Locate every blood parasite and identify its species.
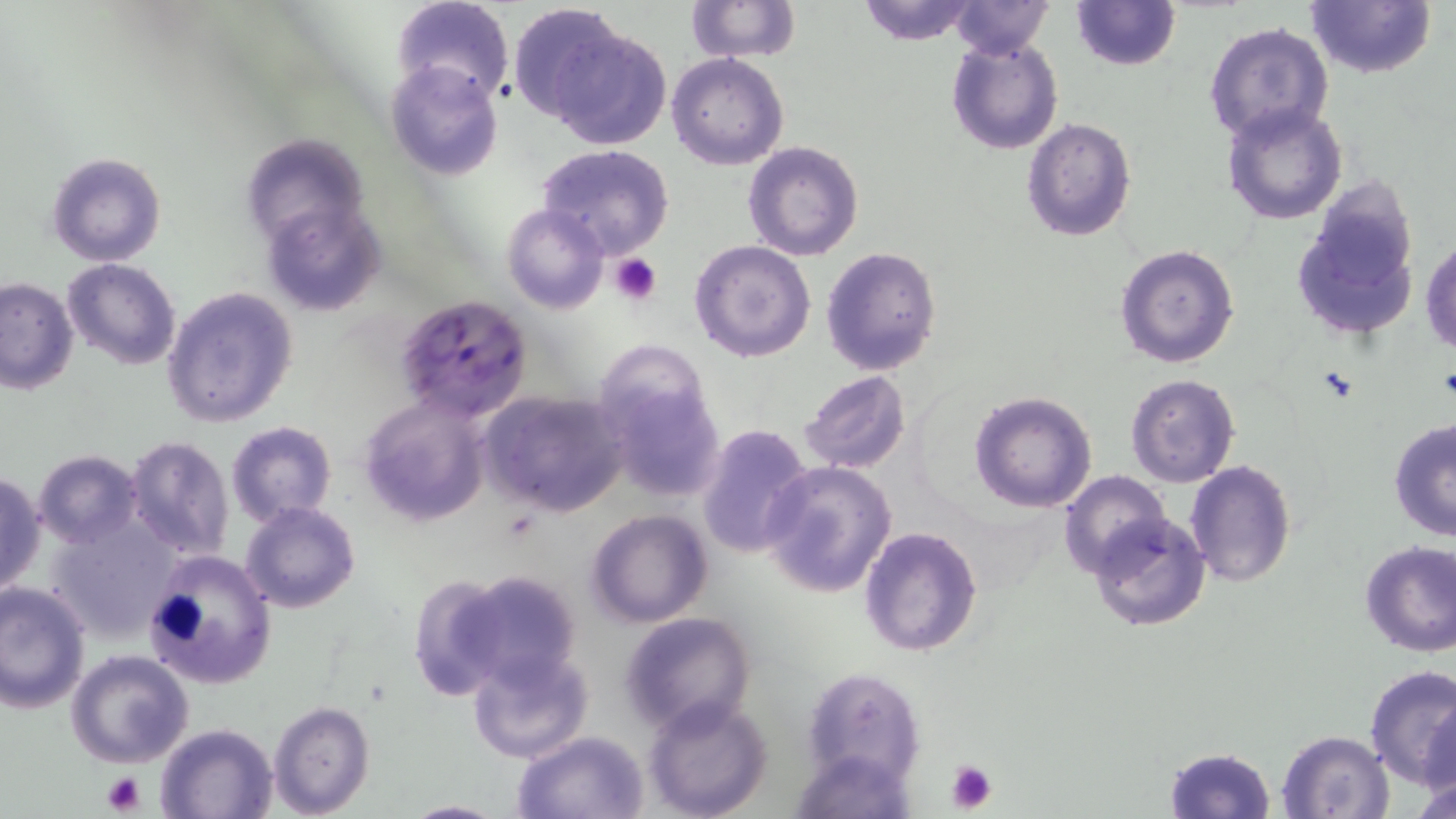
Approximate bounding boxes as [x1, y1, x2, y2] in pixels.
Plasmodium falciparum-infected red blood cells: [396, 294, 533, 422].
No Plasmodium ovale, Plasmodium malariae, Plasmodium vivax, Babesia divergens, or Trypanosoma brucei observed.

Platelet locations: [609, 253, 662, 305], [944, 758, 999, 813], [100, 771, 148, 815]. Uninfected red blood cell locations: [392, 0, 512, 107], [685, 0, 799, 63], [853, 0, 983, 46], [948, 0, 1054, 58], [1307, 0, 1435, 79], [1070, 1, 1179, 70], [505, 2, 625, 122], [1203, 22, 1334, 145], [549, 27, 671, 150], [946, 37, 1064, 155], [667, 54, 789, 170], [384, 59, 505, 182], [1222, 103, 1346, 224], [1021, 116, 1137, 242], [239, 133, 370, 253], [743, 141, 864, 261], [536, 145, 676, 260], [45, 150, 167, 267], [1292, 187, 1421, 341], [258, 201, 386, 318], [501, 203, 608, 314], [1422, 239, 1455, 355], [689, 240, 817, 363], [1115, 244, 1240, 368], [820, 246, 943, 376], [61, 258, 181, 370], [0, 274, 79, 393], [162, 287, 299, 430], [597, 348, 725, 503], [796, 371, 912, 475], [1126, 373, 1240, 487], [481, 389, 629, 517], [969, 389, 1098, 513], [359, 394, 490, 526], [1388, 418, 1456, 540], [226, 421, 337, 526], [695, 423, 816, 559], [125, 436, 234, 560], [32, 450, 143, 547], [1187, 460, 1296, 588], [760, 461, 897, 598], [1060, 470, 1172, 582], [0, 472, 46, 596], [241, 502, 361, 613], [587, 510, 713, 628], [45, 512, 184, 641], [1090, 512, 1212, 632], [859, 525, 983, 657], [1359, 541, 1456, 657], [142, 549, 277, 691], [451, 570, 584, 688], [406, 575, 518, 698], [0, 579, 91, 715], [618, 611, 758, 737], [468, 647, 594, 764], [67, 651, 193, 768], [1362, 664, 1456, 787], [802, 665, 925, 788], [643, 695, 775, 819], [1418, 696, 1456, 799], [268, 702, 375, 818], [153, 722, 279, 819], [509, 730, 649, 818], [1276, 730, 1394, 818], [791, 745, 919, 818], [1162, 746, 1277, 819], [1411, 765, 1456, 819], [395, 799, 509, 818]. Slide-level diagnosis: Plasmodium falciparum. May-Grünwald-Giemsa stain. Captured at 1000x magnification. Image is 1456×819 pixels. Optical microscopy. Single field of view. Thin blood smear.